Assess the morphology of the erythrocytes.
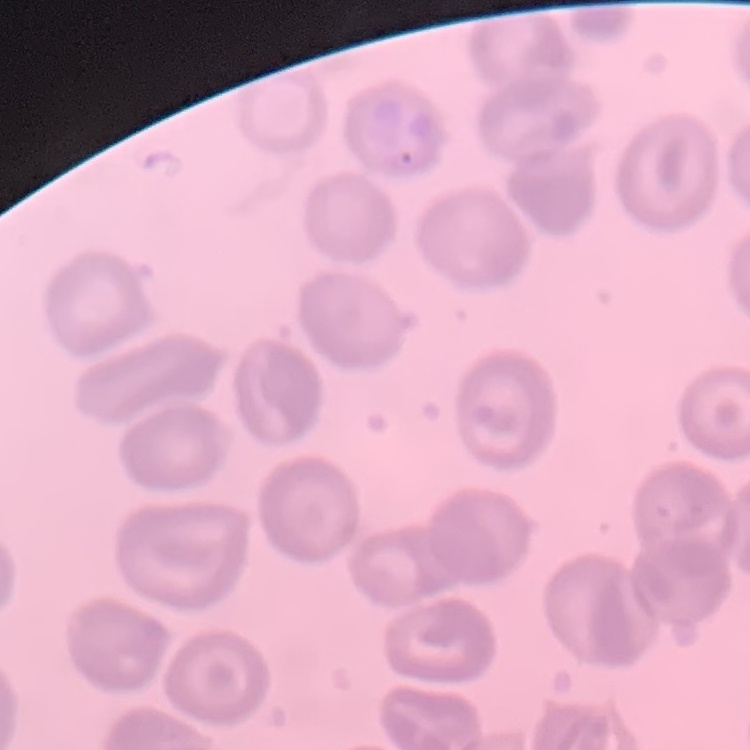
They show no rouleaux formation.

image type = square crop of a larger photomicrograph
stain = Field's or Giemsa
preparation = thin blood film